Report the malaria status of this cell.
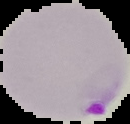

It is parasitized.

image type = segmented cell region on a black background
image size = 130×124 pixels
preparation = thin blood film